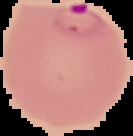
Summary:
  - Malaria status: parasitized
  - Image size: 133×136 pixels
  - Preparation: thin blood film
  - Image type: segmented cell region with the area outside set to black